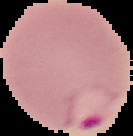
Summary:
  - Image size: 133×136 pixels
  - Malaria status: parasitized
  - Image type: segmented cell region on a black background
  - Preparation: thin blood film